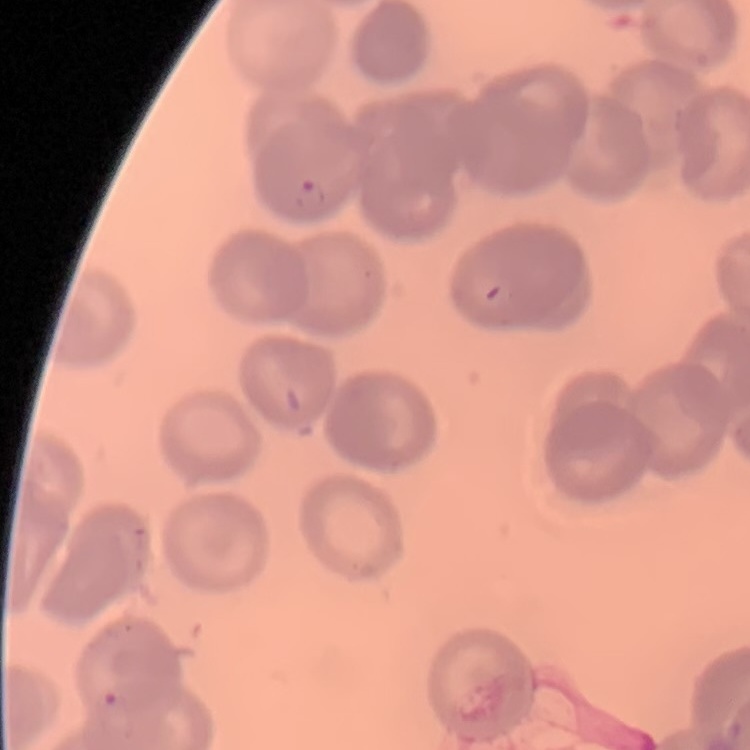 The red blood cells exhibit no rouleaux formation. Thin blood film. Square crop of a larger photomicrograph. Field's or Giemsa stain.